Assess the morphology of the red blood cells.
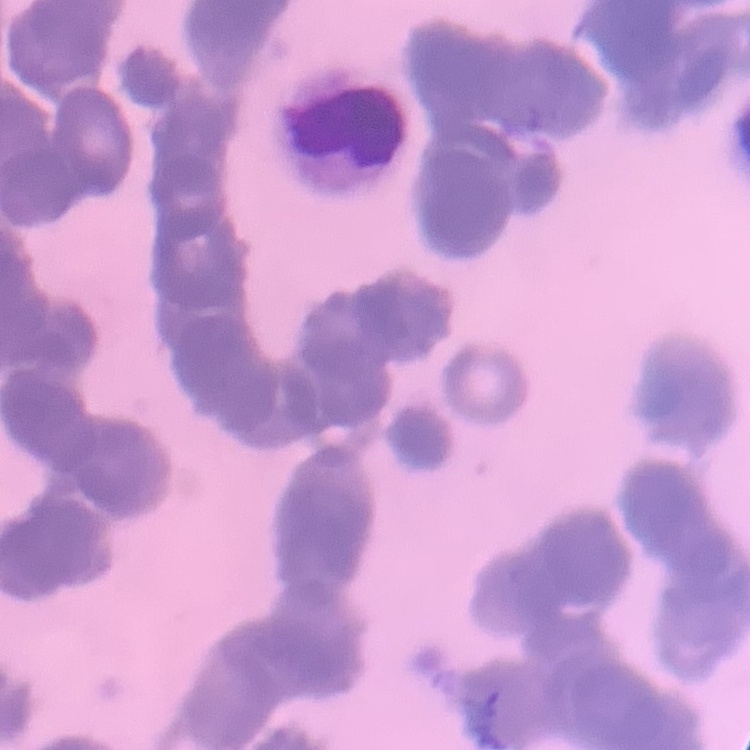
Rouleaux formation.

preparation: thin blood smear
image_type: one tile cut from a larger photomicrograph
stain: Field's or Giemsa